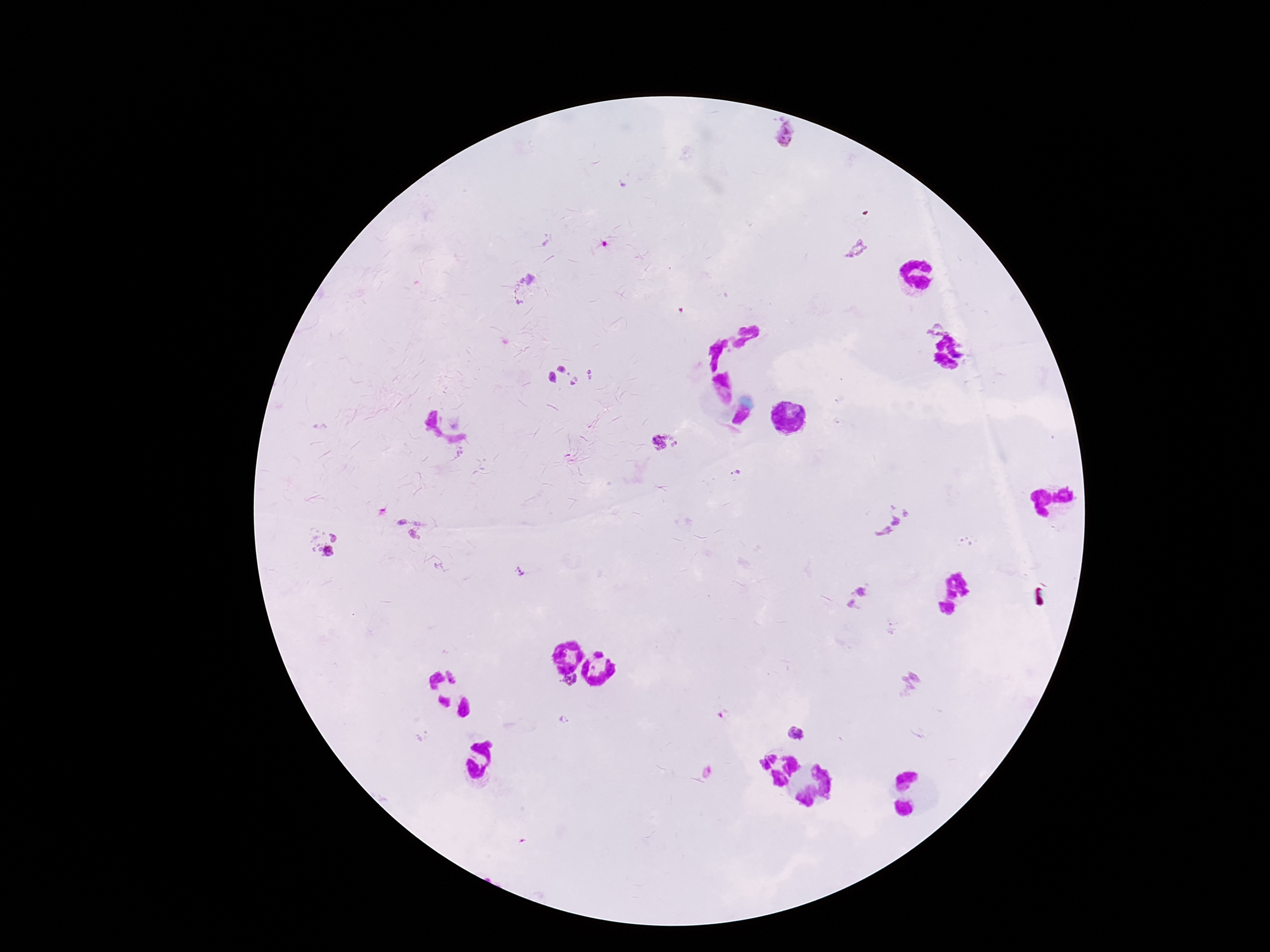
Approximate centers as [x, y] in pixels.
Summary:
  - Plasmodium parasite locations: [787, 133], [855, 248], [528, 290], [930, 327], [561, 368], [591, 373], [552, 377], [575, 382], [665, 444], [737, 472], [888, 518], [403, 521], [423, 530], [334, 536], [321, 553], [520, 572], [861, 588], [850, 604], [571, 681], [912, 683], [792, 733]
  - Magnification: 100x
  - Field of view: single
  - Patient malaria status: infected
  - Capture: smartphone camera through the microscope eyepiece
  - Stain: Giemsa
  - Preparation: thick blood film
  - Image size: 1270×952 pixels